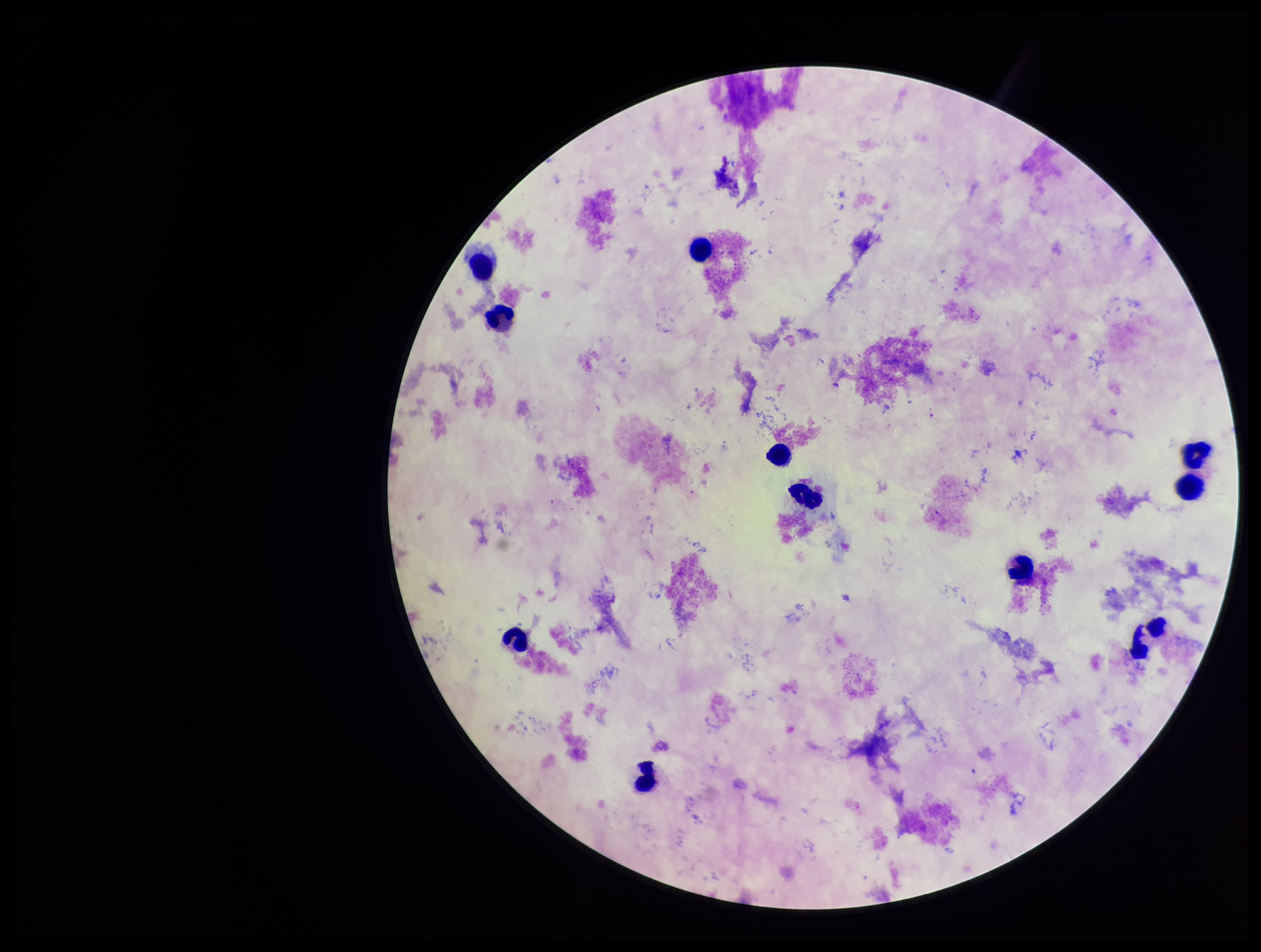
patient malaria status = positive
capture = smartphone photograph through the microscope eyepiece
field of view = single
image size = 1261×952 pixels
Plasmodium parasites = none detected
parasite count = 0
leukocyte count = 12
preparation = thick smear
stain = Giemsa
species reported for this patient = Plasmodium falciparum